Point out each Plasmodium parasite.
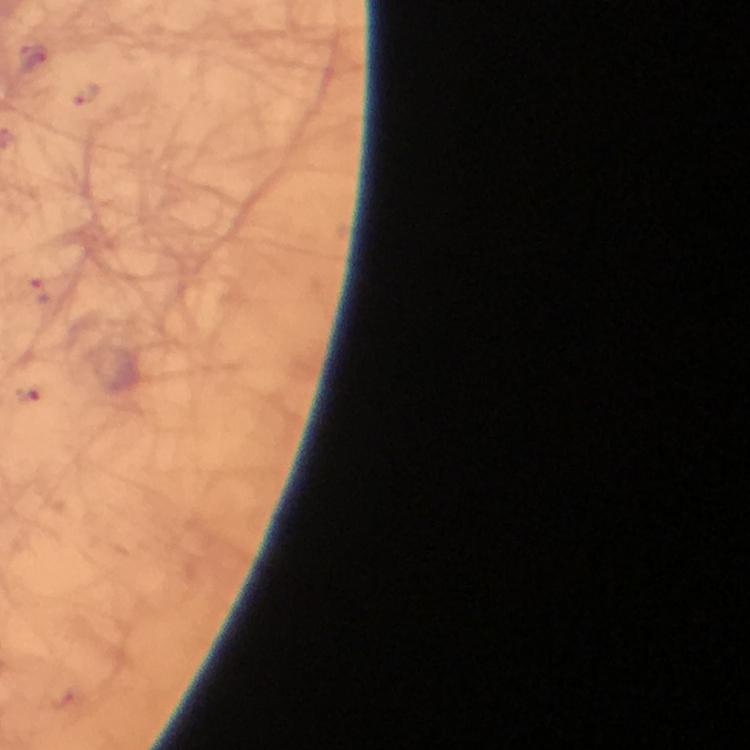

Approximate centers as (x, y) in pixels.
Plasmodium parasites: (33, 61), (26, 394).

A crop from one field of view. Image is 750×750 pixels. 100x magnification. Thick smear. From a malaria diagnostic workup. Photographed through the microscope with a smartphone camera. Giemsa stain. Immersion oil applied.